Report the malaria status.
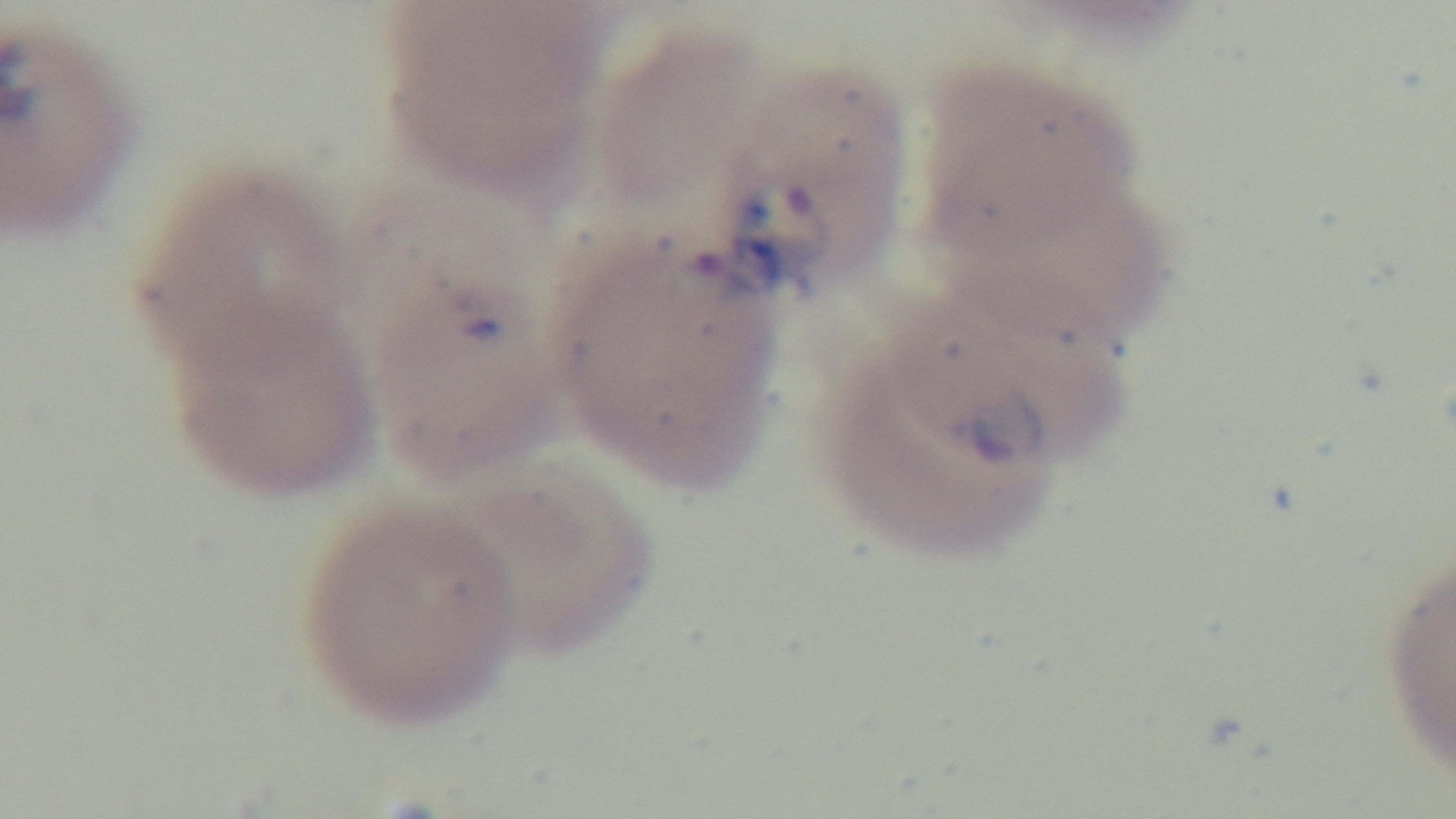

It is infected.

One field from the slide. Mounted 4K digital camera. Photomicrograph. Giemsa-stained. Preparation: thin. Oil-immersion objective, 100x.